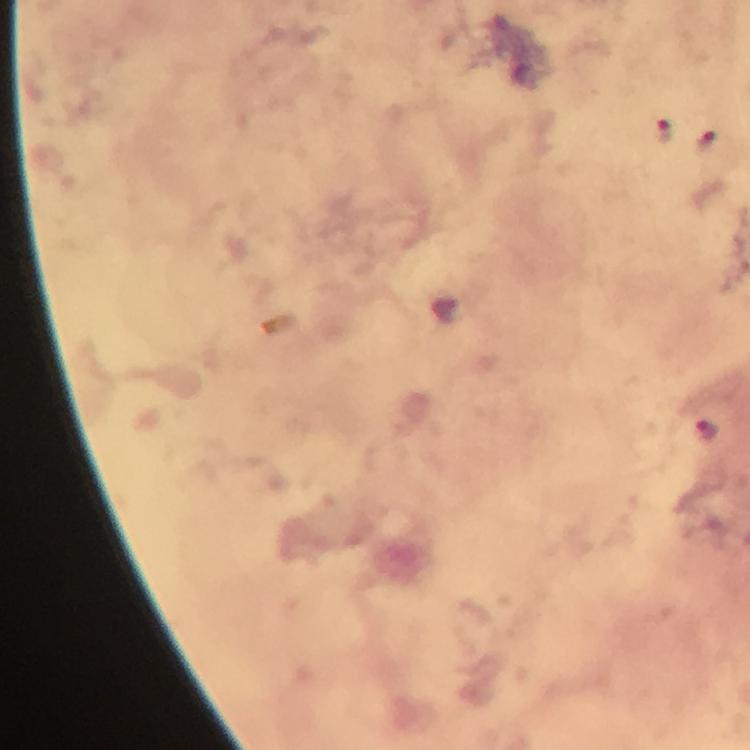
stain = Giemsa
image size = 750×750 pixels
context = from a malaria diagnostic workup
capture = smartphone camera through the microscope
magnification = 100x
Plasmodium parasite locations = approximate centers as {x, y} in pixels: {664, 129}, {709, 431}
preparation = thick blood film
cropped from = a single field of view
immersion oil = used